Classify this cell by malaria status.
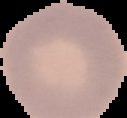

Uninfected.

Summary:
  - Image type: segmented cell region on a black background
  - Image size: 127×118 pixels
  - Preparation: thin blood smear